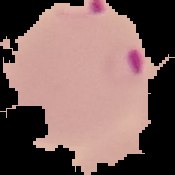 The area outside the segmented cell region is set to black. Result: Plasmodium parasites detected. From a thin blood smear. Image is 175×175 pixels.